Comment on the morphology of the erythrocytes.
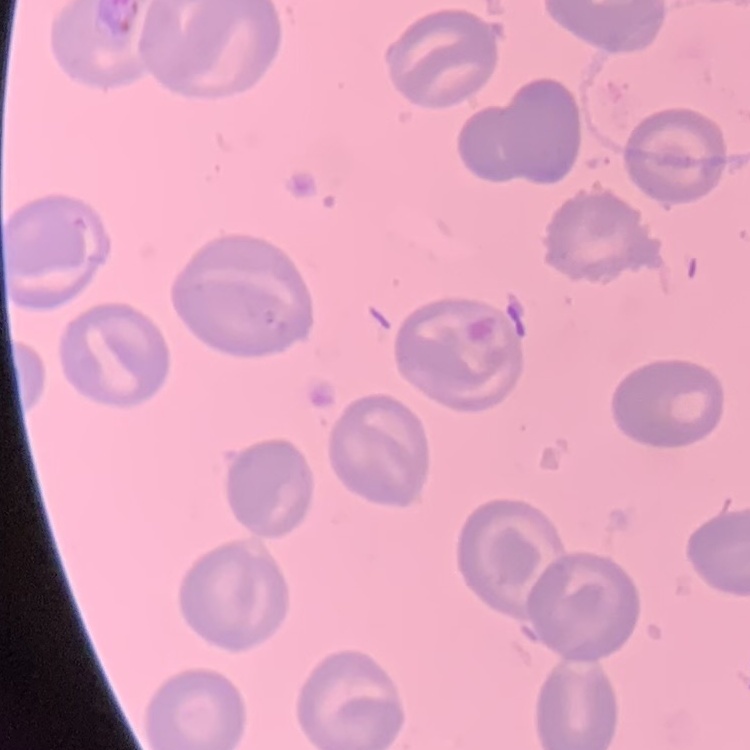
No rouleaux formation.

preparation: thin blood film
stain: Field's or Giemsa
image_type: one tile cut from a larger photomicrograph